Locate every Plasmodium parasite and every leukocyte.
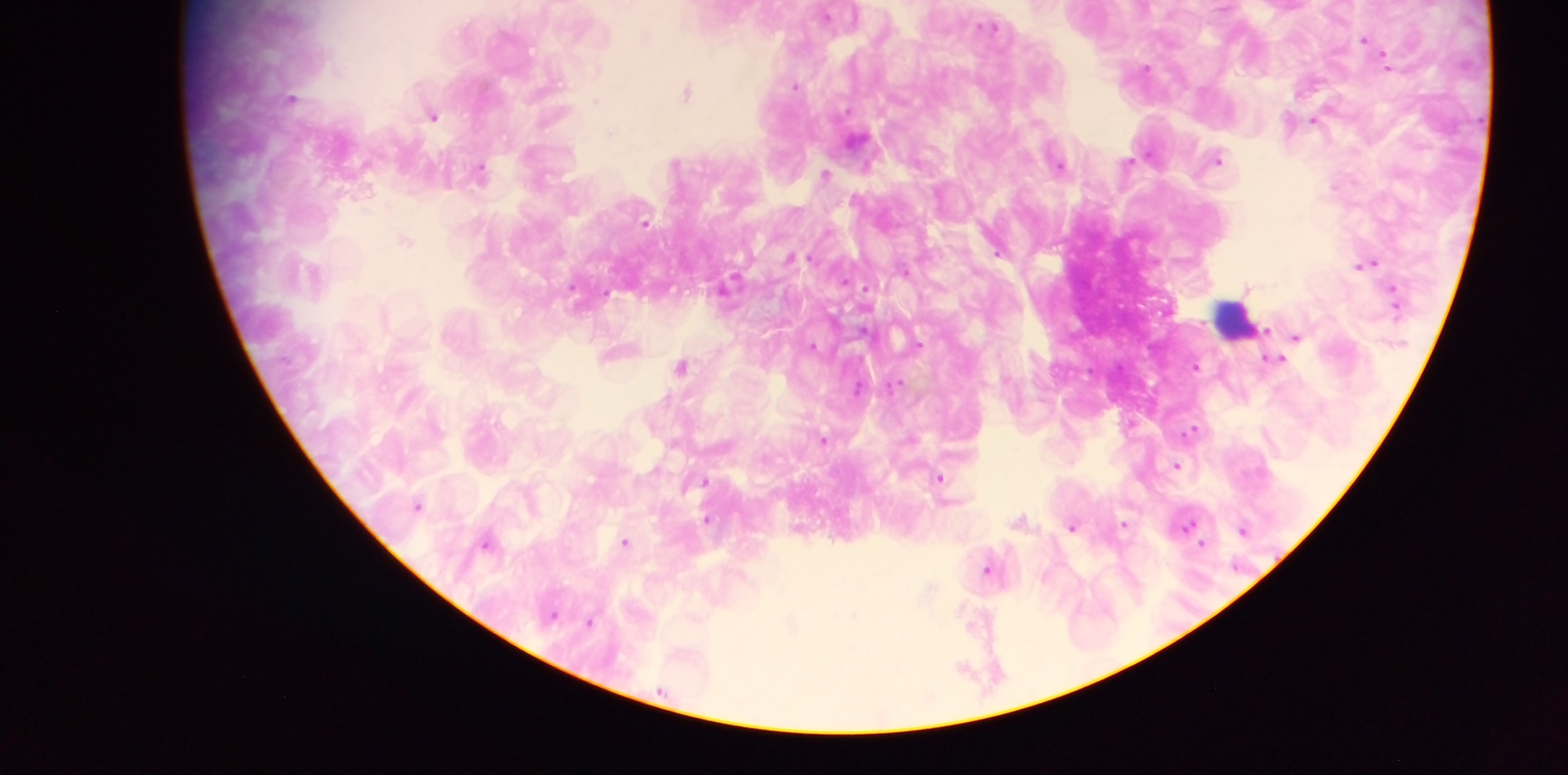
Approximate centers as [x, y] in pixels.
Plasmodium parasites: [1363, 36], [1389, 62], [1146, 66], [798, 83], [689, 89], [434, 116], [1220, 158], [1061, 162], [826, 173], [789, 256], [1372, 261], [1362, 263], [1250, 285], [575, 289], [835, 316], [1297, 336], [921, 338], [815, 343], [1196, 367], [896, 384], [858, 389], [1191, 432], [826, 437], [1180, 465], [941, 477], [951, 502], [708, 517], [1018, 518], [1188, 523], [1072, 528], [1243, 528], [625, 540], [1202, 542], [486, 543], [985, 570], [554, 613], [591, 619].
Leukocytes: [1231, 316].

field of view = single
preparation = thick blood smear
country = Ghana
capture = mobile-phone photograph through a microscope
image size = 1568×775 pixels